Comment on the morphology of the red blood cells.
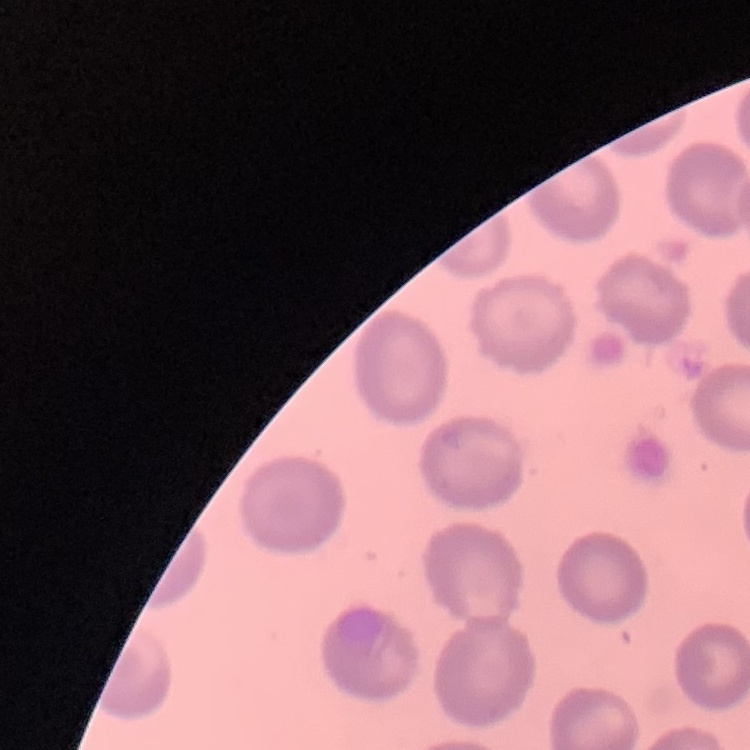

No rouleaux formation.

Field's or Giemsa stain. One tile cut from a larger photomicrograph. Thin blood smear.